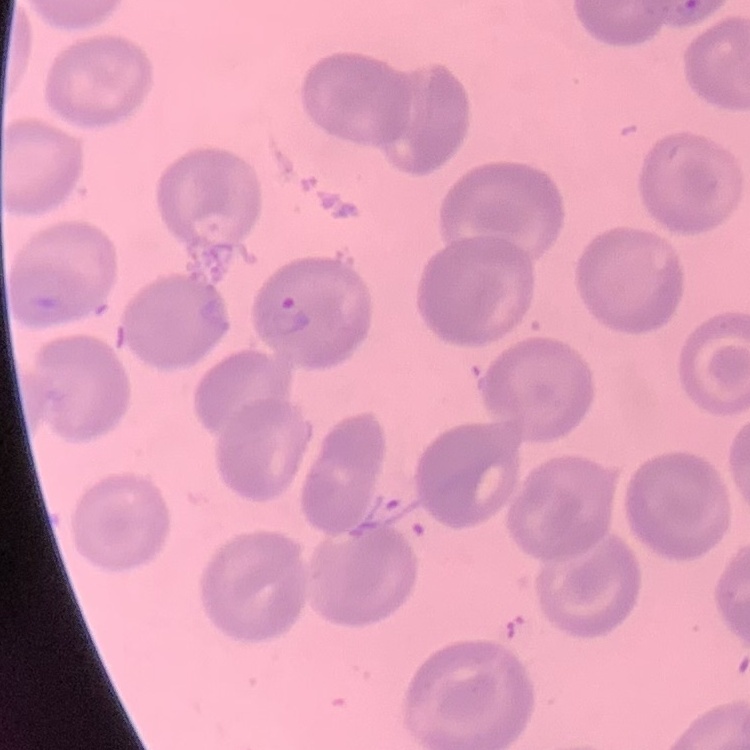
Summary:
  - Red blood cell morphology: no rouleaux formation
  - Image type: square crop of a larger photomicrograph
  - Preparation: thin peripheral smear
  - Stain: Field's or Giemsa